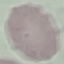

result = negative for malaria parasites
stain = Giemsa
preparation = thin blood smear
image type = automatically extracted cell patch, resized to 64 × 64 pixels
capture = smartphone camera at the microscope eyepiece